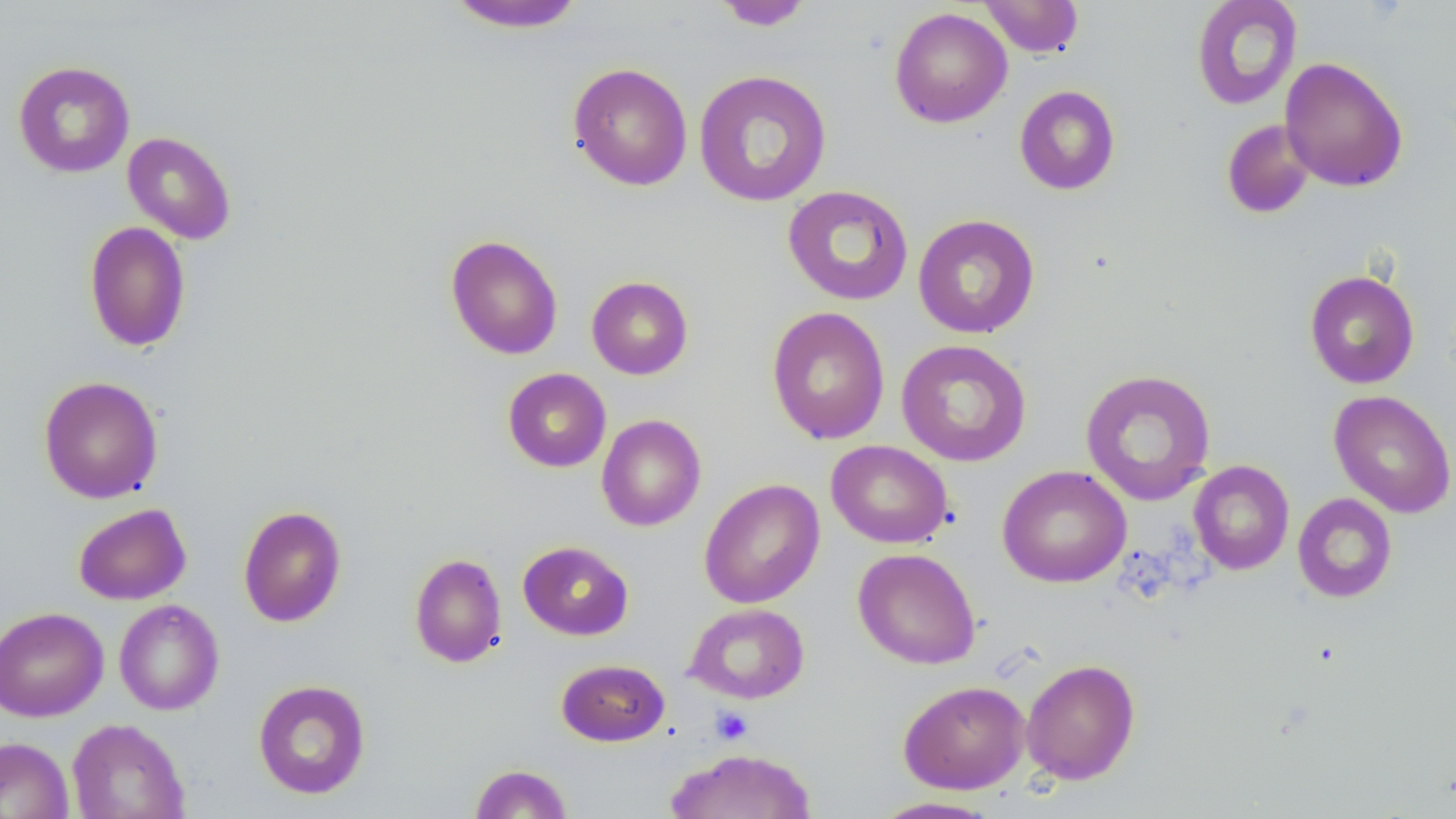

slide-level diagnosis = no evidence of blood parasites
image size = 1456×819 pixels
field of view = single
modality = optical microscopy
uninfected red blood cell locations = approximate bounding boxes as [x1, y1, x2, y2] in pixels: [978, 0, 1085, 58], [1190, 0, 1303, 110], [443, 1, 586, 33], [712, 1, 814, 30], [889, 7, 1012, 128], [1279, 57, 1409, 192], [13, 60, 136, 179], [567, 62, 693, 191], [693, 69, 832, 207], [1013, 85, 1121, 196], [1221, 119, 1316, 220], [122, 131, 236, 244], [782, 185, 913, 306], [912, 213, 1040, 339], [84, 221, 191, 352], [446, 234, 563, 360], [1304, 269, 1420, 389], [586, 275, 694, 380], [767, 306, 890, 444], [896, 339, 1032, 467], [502, 368, 611, 472], [1080, 368, 1217, 506], [39, 375, 163, 503], [1329, 390, 1456, 518], [596, 414, 706, 532], [826, 440, 953, 549], [1188, 460, 1294, 575], [997, 465, 1132, 588], [699, 479, 825, 608], [1293, 493, 1398, 602], [73, 503, 192, 605], [238, 505, 347, 627], [518, 540, 634, 640], [852, 547, 981, 670], [409, 553, 507, 668], [113, 599, 225, 715], [685, 602, 810, 704], [0, 607, 109, 722], [1021, 658, 1141, 784], [556, 659, 669, 746], [252, 679, 371, 800], [898, 680, 1030, 794], [67, 718, 190, 819], [0, 736, 74, 819], [666, 747, 817, 819], [469, 763, 574, 818], [869, 796, 1005, 818]
platelet locations = approximate bounding boxes as [x1, y1, x2, y2] in pixels: [711, 706, 753, 745]
stain = May-Grünwald-Giemsa
preparation = thin blood film
magnification = 1000x